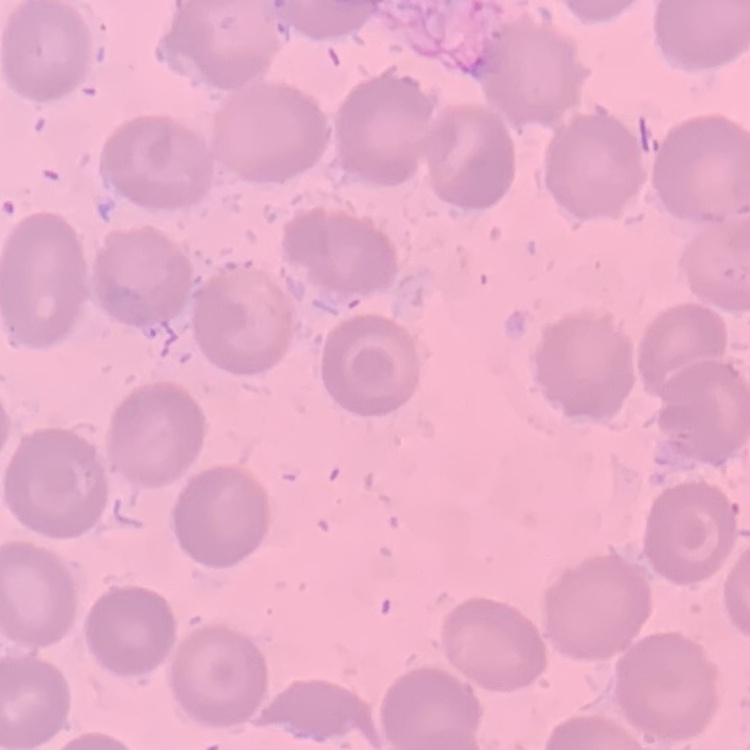

erythrocyte morphology = no rouleaux formation
image type = square crop of a larger photomicrograph
stain = Field's or Giemsa
preparation = thin peripheral smear